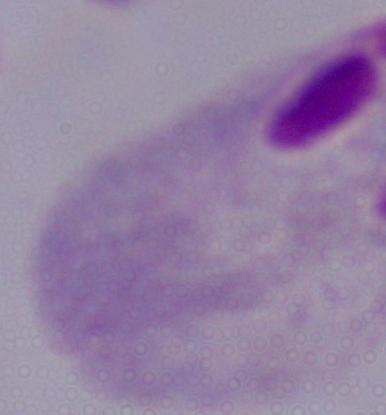

Summary:
  - Magnification: 1000x
  - Modality: photomicrograph
  - Identification: trichomonad